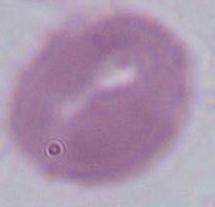
Summary:
  - Modality: photomicrograph
  - Magnification: 1000x
  - Identification: red blood cell